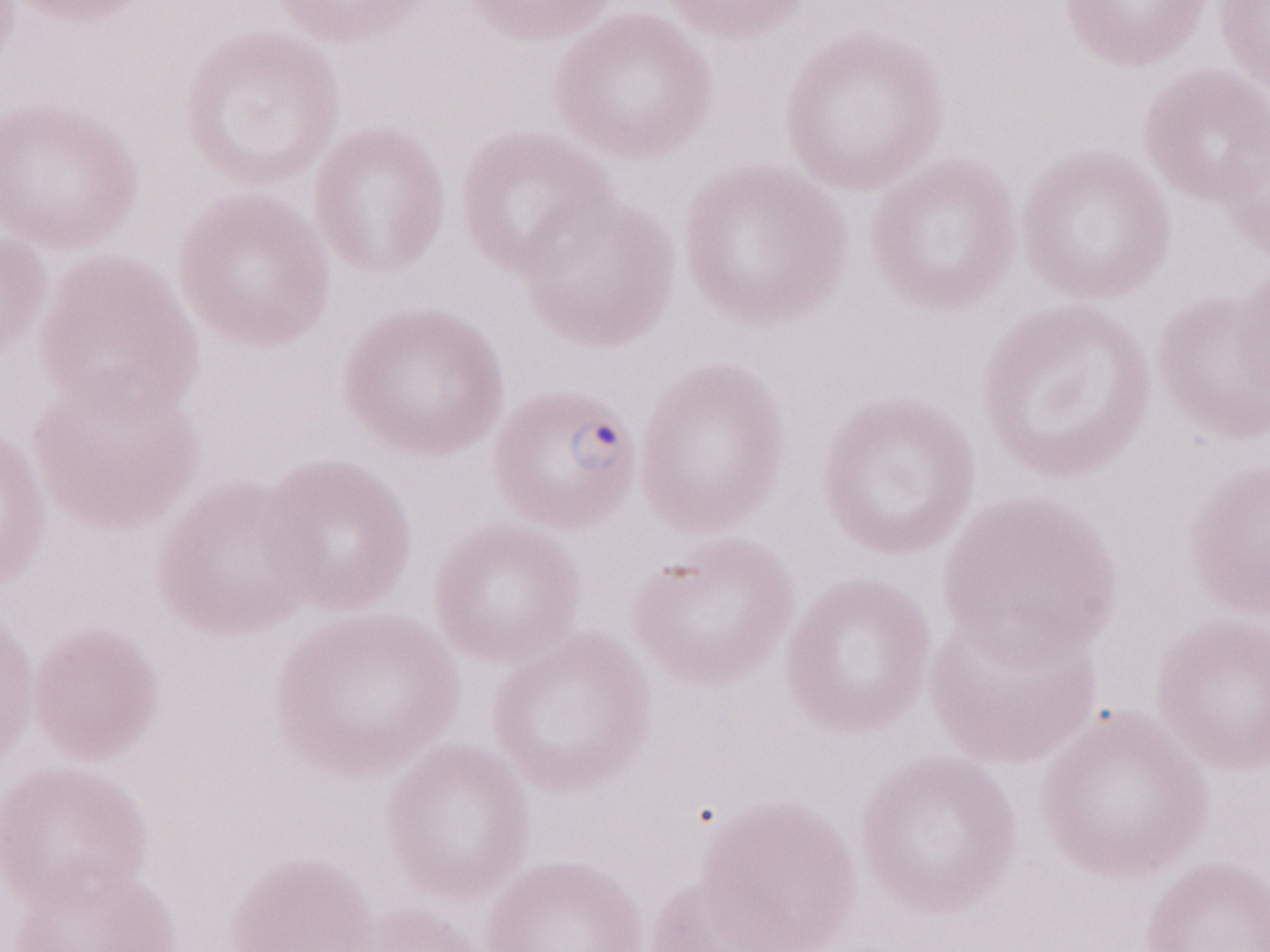 Magnification: 1,000x. One field of this slide. May-Grünwald-Giemsa stain. Olympus BX43 microscope, Olympus DP73 camera. Image is 1270×952 pixels. Thin peripheral-blood smear. Patient-level malaria diagnosis: positive.